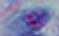

{
  "modality": "micrograph",
  "magnification": "1000x",
  "identification": "Toxoplasma gondii"
}